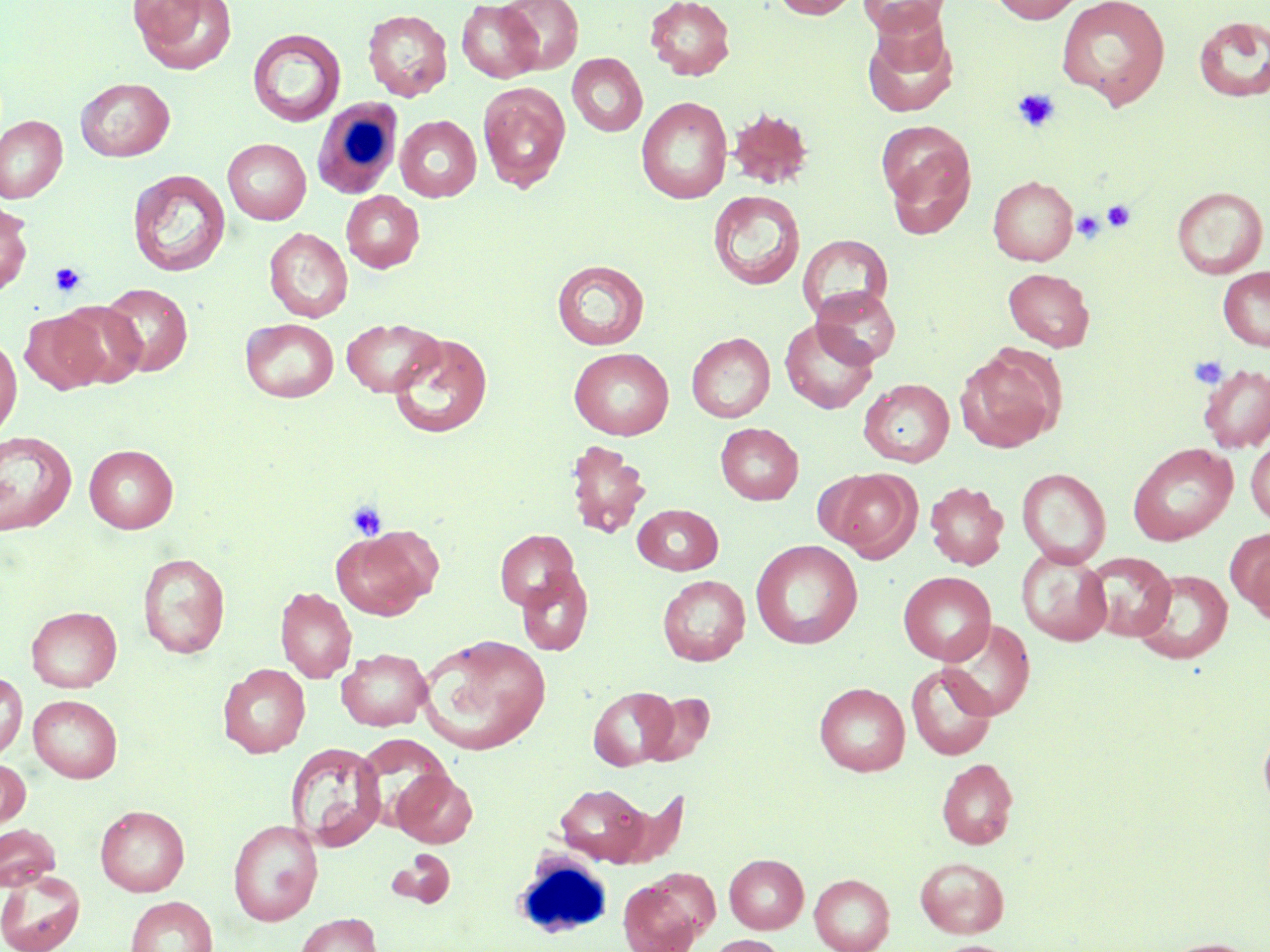

Approximate bounding boxes as named x1/y1/x2/y2 corners in pixels. Platelet locations (subset): (x1=1012, y1=89, x2=1060, y2=132), (x1=1102, y1=200, x2=1136, y2=232), (x1=1072, y1=210, x2=1106, y2=245), (x1=49, y1=262, x2=87, y2=298), (x1=1188, y1=355, x2=1229, y2=390), (x1=347, y1=501, x2=387, y2=540). White blood cell locations: (x1=311, y1=97, x2=403, y2=200), (x1=520, y1=849, x2=609, y2=949). Uninfected red blood cell locations (subset): (x1=131, y1=0, x2=237, y2=74), (x1=498, y1=0, x2=583, y2=75), (x1=645, y1=0, x2=735, y2=80), (x1=771, y1=0, x2=860, y2=19), (x1=859, y1=0, x2=948, y2=37), (x1=987, y1=0, x2=1087, y2=24), (x1=1055, y1=0, x2=1171, y2=109), (x1=457, y1=1, x2=543, y2=83), (x1=362, y1=8, x2=452, y2=101), (x1=1193, y1=16, x2=1270, y2=103), (x1=862, y1=17, x2=958, y2=118), (x1=247, y1=29, x2=346, y2=127), (x1=567, y1=53, x2=648, y2=136), (x1=75, y1=77, x2=175, y2=161), (x1=478, y1=81, x2=571, y2=193), (x1=636, y1=96, x2=733, y2=204), (x1=726, y1=106, x2=815, y2=190), (x1=0, y1=115, x2=67, y2=203), (x1=395, y1=115, x2=482, y2=202), (x1=876, y1=121, x2=976, y2=231), (x1=223, y1=138, x2=311, y2=224), (x1=128, y1=169, x2=231, y2=277), (x1=988, y1=175, x2=1078, y2=265), (x1=1171, y1=186, x2=1268, y2=278), (x1=342, y1=190, x2=424, y2=273), (x1=708, y1=190, x2=805, y2=290), (x1=0, y1=202, x2=33, y2=295), (x1=264, y1=227, x2=352, y2=322), (x1=797, y1=234, x2=893, y2=323), (x1=552, y1=260, x2=649, y2=350), (x1=1217, y1=267, x2=1270, y2=351), (x1=1004, y1=268, x2=1095, y2=351), (x1=99, y1=283, x2=193, y2=376), (x1=812, y1=286, x2=902, y2=367), (x1=53, y1=301, x2=149, y2=388), (x1=21, y1=310, x2=110, y2=394), (x1=240, y1=318, x2=338, y2=402), (x1=341, y1=318, x2=443, y2=397), (x1=779, y1=318, x2=878, y2=414), (x1=388, y1=332, x2=494, y2=438), (x1=687, y1=332, x2=775, y2=422), (x1=0, y1=336, x2=22, y2=438), (x1=955, y1=346, x2=1063, y2=452), (x1=569, y1=347, x2=674, y2=439), (x1=859, y1=378, x2=954, y2=467), (x1=716, y1=423, x2=803, y2=505), (x1=0, y1=430, x2=77, y2=535), (x1=1246, y1=438, x2=1270, y2=525), (x1=565, y1=439, x2=651, y2=539), (x1=1128, y1=442, x2=1237, y2=545), (x1=84, y1=444, x2=178, y2=533), (x1=820, y1=468, x2=920, y2=560), (x1=1017, y1=468, x2=1111, y2=567), (x1=925, y1=481, x2=1008, y2=570), (x1=633, y1=504, x2=723, y2=575), (x1=331, y1=525, x2=439, y2=620), (x1=495, y1=529, x2=579, y2=611), (x1=1233, y1=530, x2=1270, y2=625), (x1=750, y1=539, x2=863, y2=649), (x1=1016, y1=547, x2=1112, y2=645), (x1=138, y1=552, x2=230, y2=658), (x1=1085, y1=552, x2=1176, y2=641), (x1=516, y1=567, x2=593, y2=656), (x1=1133, y1=568, x2=1233, y2=665), (x1=898, y1=571, x2=996, y2=665), (x1=657, y1=575, x2=750, y2=665), (x1=275, y1=586, x2=357, y2=683), (x1=26, y1=606, x2=121, y2=692), (x1=938, y1=619, x2=1035, y2=720), (x1=418, y1=634, x2=551, y2=754), (x1=337, y1=648, x2=431, y2=731), (x1=218, y1=663, x2=310, y2=758), (x1=906, y1=663, x2=997, y2=760), (x1=0, y1=671, x2=27, y2=761), (x1=815, y1=682, x2=910, y2=776), (x1=588, y1=686, x2=677, y2=770), (x1=641, y1=692, x2=715, y2=766), (x1=29, y1=694, x2=123, y2=783), (x1=1258, y1=721, x2=1270, y2=815), (x1=286, y1=741, x2=386, y2=850), (x1=936, y1=758, x2=1018, y2=849), (x1=0, y1=759, x2=30, y2=829), (x1=391, y1=769, x2=477, y2=848), (x1=554, y1=782, x2=655, y2=865), (x1=95, y1=805, x2=190, y2=896), (x1=228, y1=819, x2=323, y2=925), (x1=0, y1=823, x2=61, y2=890), (x1=388, y1=849, x2=455, y2=908), (x1=725, y1=854, x2=808, y2=933), (x1=915, y1=856, x2=1009, y2=937), (x1=0, y1=870, x2=85, y2=952), (x1=810, y1=873, x2=895, y2=952), (x1=618, y1=877, x2=704, y2=952), (x1=125, y1=896, x2=218, y2=952), (x1=295, y1=913, x2=382, y2=952), (x1=706, y1=935, x2=786, y2=952), (x1=1160, y1=937, x2=1261, y2=952), (x1=930, y1=940, x2=1018, y2=952). Slide-level diagnosis: no evidence of blood parasites. One field of a larger specimen. Captured at 1000x magnification. Image is 1270×952 pixels. May-Grünwald-Giemsa-stained preparation. Thin blood film. Optical microscopy.